Report the malaria status of this cell.
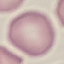
It is uninfected.

Thin blood smear. Giemsa-stained preparation. Automatically extracted cell patch, resized to 64 × 64 pixels. Photographed with a smartphone camera at the microscope eyepiece.